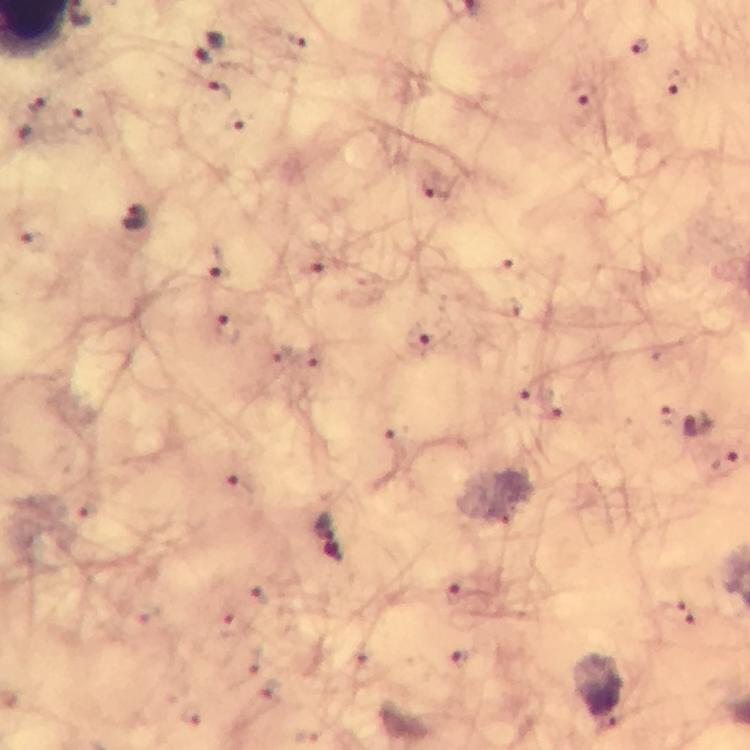
{
  "capture": "smartphone mounted on the microscope",
  "stain": "Giemsa",
  "malaria_parasite_locations": "approximate centers as (x, y) in pixels: (210, 46), (639, 46), (673, 80), (217, 92), (583, 93), (35, 98), (82, 121), (239, 125), (429, 191), (135, 221), (32, 243), (216, 264), (309, 268), (505, 270), (228, 328), (418, 339), (278, 357), (310, 360), (520, 404), (549, 404), (667, 416), (702, 423), (394, 443), (723, 460), (239, 486), (320, 523), (333, 553), (257, 595), (457, 599), (678, 612), (230, 626), (463, 658)",
  "image_size": "750×750 pixels",
  "cropped_from": "one field of view",
  "context": "from a diagnostic examination for malaria",
  "preparation": "thick blood film",
  "magnification": "100x",
  "immersion_oil": "applied"
}